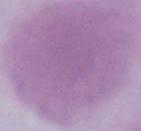

1000x magnification. An erythrocyte is seen. Photomicrograph.